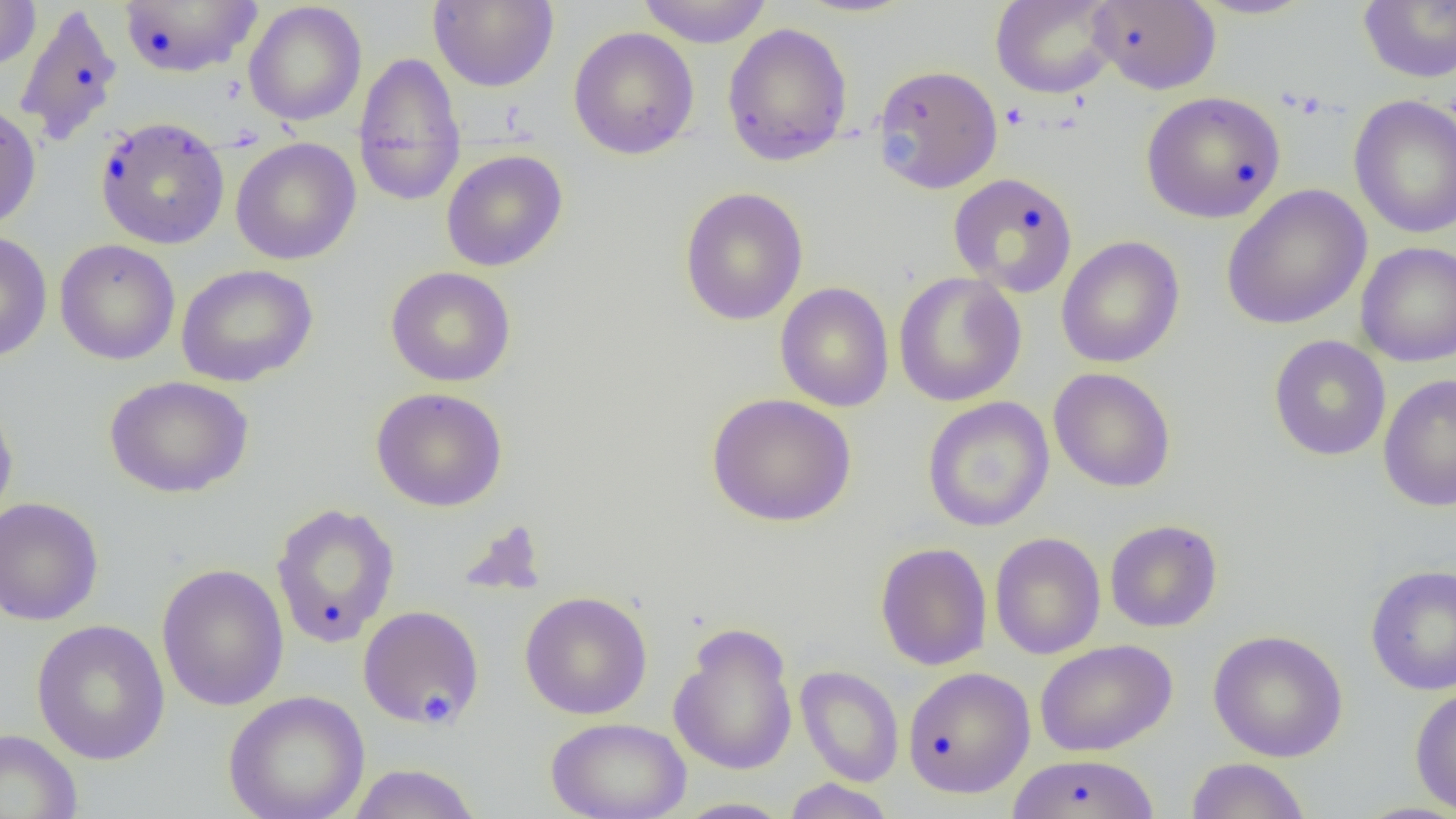
slide_level_diagnosis: no evidence of blood parasites
preparation: thin blood smear
platelet_locations: 'approximate bounding boxes as (x1, y1, x2, y2) in pixels: (420, 688, 458, 723)'
magnification: 1000x
image_size: 1456×819 pixels
field_of_view: single
modality: optical microscopy
uninfected_red_blood_cell_locations: 'approximate bounding boxes as (x1, y1, x2, y2) in pixels: (0, 0, 41, 71), (428, 0, 559, 92), (637, 0, 774, 47), (990, 0, 1118, 98), (1188, 0, 1319, 20), (1358, 0, 1456, 84), (118, 1, 262, 78), (1088, 1, 1220, 94), (243, 2, 367, 127), (13, 3, 123, 147), (721, 22, 853, 167), (568, 26, 700, 160), (353, 51, 466, 207), (872, 64, 1003, 194), (1141, 91, 1286, 224), (1349, 94, 1456, 240), (0, 102, 41, 232), (95, 116, 230, 250), (230, 137, 361, 265), (441, 149, 568, 272), (948, 172, 1078, 297), (1221, 184, 1372, 330), (679, 186, 809, 326), (0, 231, 52, 363), (1056, 235, 1185, 368), (54, 239, 180, 365), (1355, 241, 1456, 367), (54, 249, 316, 369), (176, 264, 318, 387), (385, 267, 516, 387), (893, 272, 1027, 407), (775, 283, 894, 412), (1268, 335, 1391, 461), (1048, 367, 1176, 492), (1378, 374, 1456, 512), (104, 375, 253, 498), (371, 387, 508, 511), (0, 393, 18, 530), (706, 393, 857, 527), (922, 396, 1054, 532), (0, 497, 104, 627), (270, 502, 401, 648), (1105, 519, 1223, 632), (989, 532, 1106, 660), (875, 542, 992, 671), (156, 563, 289, 712), (1365, 564, 1456, 696), (519, 591, 653, 720), (358, 605, 485, 730), (31, 619, 170, 765), (668, 621, 799, 776), (1207, 629, 1348, 762), (1035, 639, 1177, 757), (795, 665, 904, 786), (903, 667, 1035, 798), (1410, 686, 1456, 816), (223, 690, 370, 819), (545, 717, 691, 819), (0, 728, 83, 819), (1006, 754, 1161, 819), (1185, 757, 1312, 819), (345, 763, 483, 819), (782, 778, 896, 819), (672, 797, 794, 818)'